Identify the preparation type.
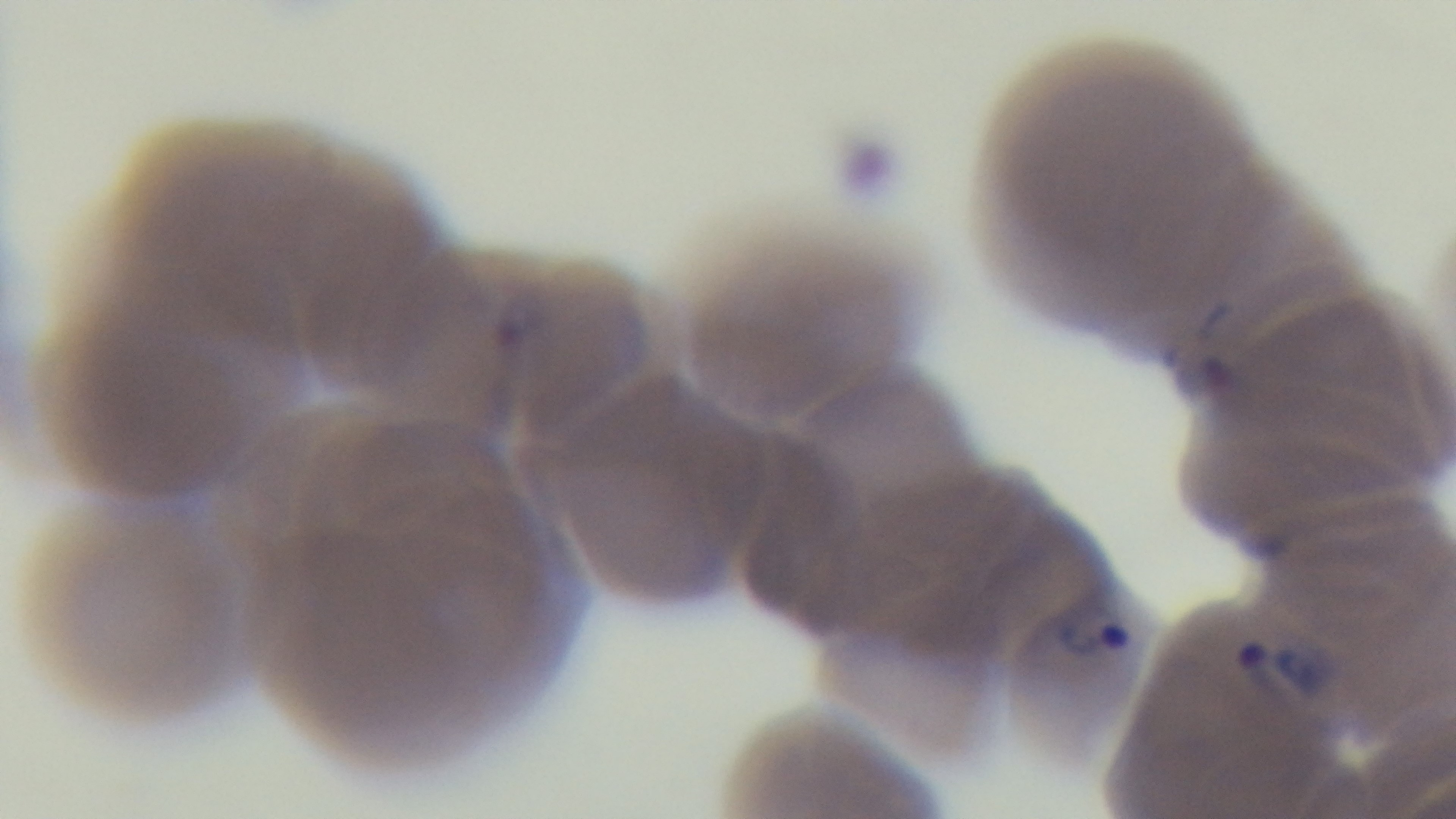

A thin smear.

capture = mounted 4K digital camera
modality = light microscopy
objective = 100x oil immersion
field of view = single
stain = Giemsa
malaria status = positive